Identify the parasite.
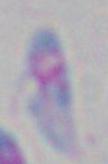
This is Toxoplasma gondii.

Summary:
  - Modality: photomicrograph
  - Magnification: 1000x